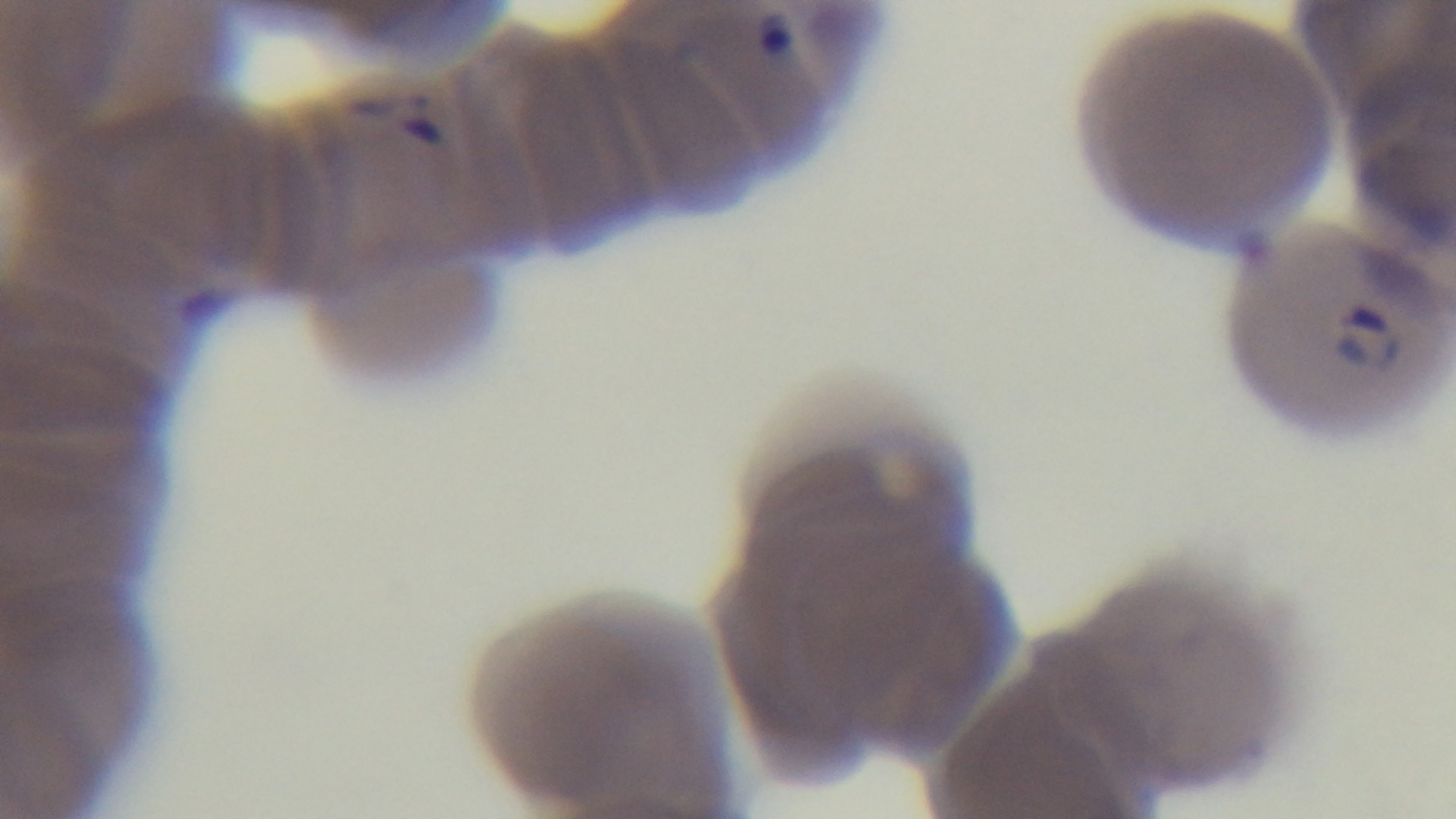
preparation = thin
malaria status = infected
stain = Giemsa
field of view = one from the slide
capture = mounted 4K digital camera
objective = 100x oil immersion
modality = light microscopy